Outline platelets.
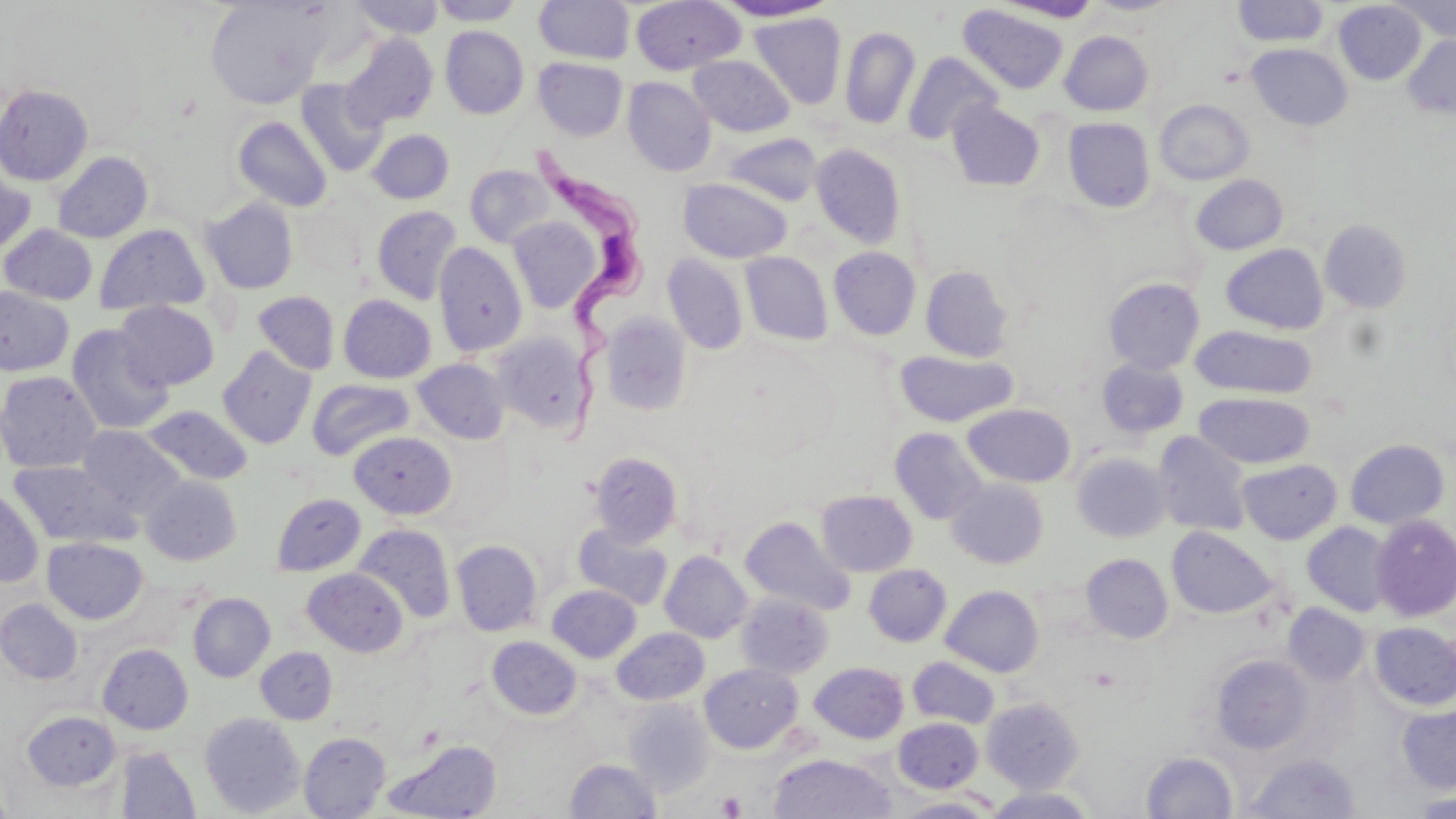

Approximate bounding boxes as (x1,y1)-(x2,y2) corner pairs in pixels.
Platelets: (716,791)-(747,818).

Uninfected red blood cell locations: (204,0)-(330,109), (348,0)-(444,39), (429,0)-(526,26), (713,0)-(837,22), (1390,0)-(1456,42), (534,1)-(635,64), (631,1)-(746,74), (993,1)-(1103,23), (1231,1)-(1329,47), (1334,1)-(1426,84), (958,5)-(1068,95), (749,12)-(847,109), (440,26)-(529,119), (840,26)-(920,129), (1060,31)-(1154,115), (340,33)-(439,129), (1403,35)-(1456,118), (1247,43)-(1352,131), (902,51)-(1002,146), (688,55)-(795,137), (533,57)-(627,141), (623,77)-(715,176), (295,79)-(387,177), (0,84)-(93,186), (1154,99)-(1254,185), (947,100)-(1046,191), (232,115)-(332,212), (1063,117)-(1155,212), (367,128)-(454,204), (724,133)-(823,206), (811,143)-(907,249), (52,151)-(153,243), (0,163)-(36,259), (465,164)-(555,248), (1190,174)-(1288,255), (678,177)-(792,263), (201,198)-(299,294), (372,205)-(463,304), (507,216)-(601,313), (1319,219)-(1413,314), (93,223)-(210,316), (1,224)-(98,305), (433,242)-(527,357), (1221,243)-(1329,334), (829,247)-(921,340), (740,251)-(832,345), (662,253)-(749,355), (920,265)-(1015,362), (1103,278)-(1205,374), (0,286)-(74,377), (253,290)-(341,375), (338,294)-(436,383), (114,300)-(219,391), (600,313)-(692,416), (67,324)-(173,434), (1191,325)-(1316,399), (494,331)-(594,433), (217,345)-(317,449), (895,350)-(1017,427), (413,358)-(510,444), (1097,358)-(1189,438), (0,371)-(102,473), (307,378)-(415,460), (1194,392)-(1314,468), (142,404)-(253,485), (963,404)-(1076,488), (77,425)-(184,515), (890,427)-(988,524), (349,431)-(456,519), (1152,431)-(1253,537), (1345,439)-(1449,529), (589,452)-(683,547), (1072,452)-(1172,542), (1237,459)-(1342,544), (8,460)-(140,548), (142,475)-(242,565), (946,479)-(1049,569), (0,486)-(43,588), (816,490)-(917,576), (272,493)-(366,576), (1371,515)-(1456,621), (740,516)-(856,615), (1303,521)-(1395,616), (353,523)-(455,623), (573,523)-(674,609), (1167,527)-(1276,619), (42,537)-(148,624), (451,539)-(542,636), (660,551)-(752,643), (1081,553)-(1173,643), (864,564)-(951,646), (302,567)-(408,656), (546,585)-(641,662), (941,585)-(1044,677), (188,592)-(275,682), (737,593)-(834,679), (0,599)-(83,684), (1283,604)-(1370,686), (1370,622)-(1456,711), (612,627)-(709,705), (487,636)-(582,719), (97,644)-(193,734), (255,647)-(338,724), (1210,654)-(1314,754), (908,656)-(1000,728), (809,662)-(908,743), (699,663)-(803,752), (982,697)-(1084,792), (624,700)-(713,796), (1397,703)-(1456,794), (22,710)-(122,792), (200,712)-(305,817), (894,718)-(983,793), (299,732)-(390,818), (384,740)-(502,819), (115,746)-(201,818), (1141,751)-(1239,818), (769,752)-(895,818), (1243,753)-(1361,818), (565,758)-(662,818), (0,784)-(15,819), (983,787)-(1097,818), (1413,791)-(1456,817), (896,795)-(1001,817). Trypanosoma brucei locations: (511,144)-(639,444). Slide-level diagnosis: Trypanosoma brucei. May-Grünwald-Giemsa-stained preparation. 1000x magnification. Thin blood film. Light microscopy. One field of a larger specimen. Image is 1456×819 pixels.